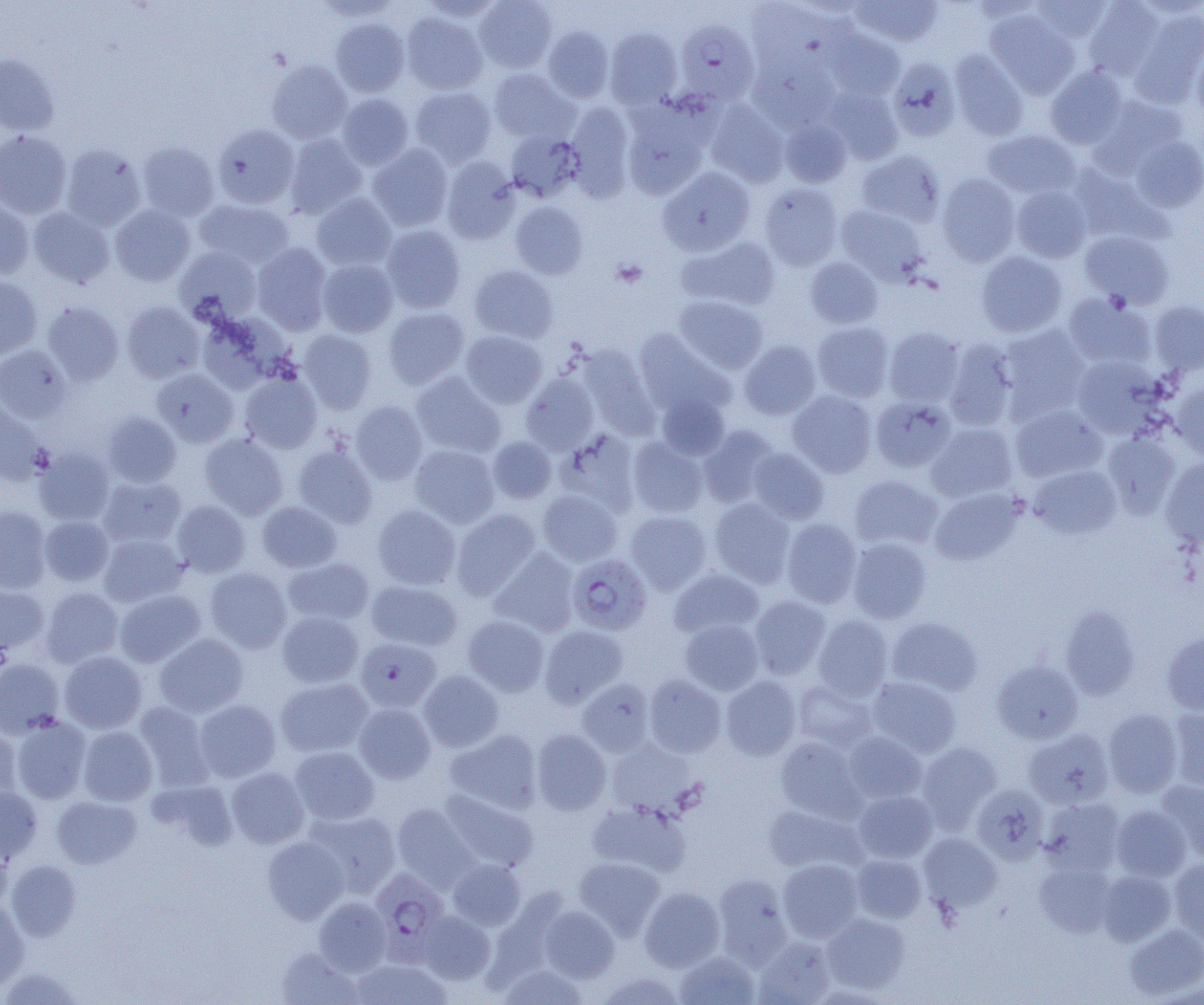 Approximate bounding boxes as [x1, y1, x2, y2] in pixels. Plasmodium falciparum-infected red blood cell locations: [674, 19, 760, 106], [566, 554, 652, 636], [355, 638, 441, 713], [369, 869, 449, 962]. Uninfected red blood cell locations: [418, 0, 502, 22], [474, 0, 557, 73], [852, 0, 943, 47], [1031, 0, 1112, 43], [1083, 1, 1164, 79], [745, 2, 834, 74], [1131, 8, 1204, 106], [985, 9, 1080, 98], [401, 12, 488, 94], [330, 18, 410, 97], [543, 26, 614, 102], [822, 26, 905, 101], [604, 27, 683, 109], [1191, 45, 1204, 121], [950, 50, 1029, 141], [749, 52, 839, 132], [0, 54, 60, 135], [887, 57, 962, 142], [266, 60, 352, 143], [1046, 66, 1128, 149], [488, 68, 577, 143], [409, 87, 496, 167], [823, 87, 904, 164], [337, 94, 413, 169], [1090, 94, 1188, 176], [705, 100, 790, 188], [565, 101, 635, 199], [622, 104, 710, 199], [780, 118, 852, 188], [213, 124, 299, 208], [982, 129, 1080, 199], [0, 130, 72, 218], [505, 130, 584, 202], [284, 134, 366, 219], [1130, 135, 1204, 212], [137, 142, 219, 220], [61, 144, 146, 231], [368, 144, 452, 231], [856, 150, 945, 226], [441, 157, 520, 244], [1068, 163, 1168, 245], [658, 166, 755, 256], [936, 174, 1020, 266], [759, 183, 844, 271], [1011, 185, 1092, 263], [312, 193, 396, 271], [0, 198, 34, 279], [194, 199, 294, 270], [511, 201, 588, 279], [110, 204, 195, 286], [836, 204, 927, 283], [28, 207, 114, 288], [381, 224, 466, 313], [1079, 230, 1173, 307], [677, 237, 781, 311], [252, 242, 332, 334], [175, 247, 261, 324], [975, 251, 1067, 337], [805, 257, 883, 328], [318, 259, 398, 337], [469, 264, 558, 343], [0, 276, 42, 360], [1062, 292, 1157, 370], [674, 295, 768, 374], [1149, 300, 1204, 375], [43, 301, 124, 385], [122, 301, 204, 383], [383, 307, 470, 389], [195, 311, 289, 393], [812, 322, 893, 402], [999, 324, 1091, 419], [884, 327, 965, 406], [299, 329, 377, 414], [633, 329, 734, 419], [460, 330, 547, 408], [942, 338, 1018, 430], [739, 340, 821, 420], [0, 345, 71, 422], [576, 345, 659, 436], [1072, 355, 1164, 438], [151, 369, 239, 446], [240, 372, 322, 454], [411, 372, 505, 458], [521, 373, 599, 453], [1170, 382, 1204, 459], [787, 389, 877, 477], [656, 392, 730, 460], [871, 396, 956, 472], [351, 400, 427, 485], [0, 402, 48, 484], [1010, 404, 1108, 483], [103, 412, 181, 487], [927, 422, 1017, 502], [698, 425, 780, 507], [557, 429, 641, 516], [1101, 432, 1180, 518], [199, 433, 288, 519], [488, 436, 557, 503], [627, 437, 708, 517], [293, 444, 377, 529], [410, 444, 499, 527], [33, 447, 115, 525], [748, 448, 829, 524], [1161, 457, 1204, 551], [1028, 464, 1121, 540], [849, 475, 942, 550], [98, 476, 186, 547], [930, 488, 1023, 565], [538, 489, 622, 566], [710, 498, 795, 587], [172, 500, 250, 577], [257, 501, 341, 573], [372, 504, 460, 590], [0, 505, 51, 593], [452, 509, 541, 600], [625, 510, 713, 594], [40, 516, 113, 585], [781, 518, 862, 608], [99, 534, 187, 606], [847, 537, 932, 623], [489, 548, 580, 636], [283, 558, 375, 626], [205, 567, 291, 652], [668, 568, 763, 639], [366, 580, 463, 651], [0, 585, 48, 654], [40, 587, 123, 667], [114, 589, 206, 667], [749, 595, 831, 679], [1059, 605, 1140, 700], [277, 611, 364, 688], [462, 615, 549, 696], [812, 615, 893, 700], [886, 617, 983, 696], [679, 618, 763, 695], [539, 625, 628, 707], [1162, 631, 1204, 716], [154, 633, 248, 717], [59, 651, 147, 733], [0, 659, 64, 737], [992, 660, 1083, 744], [418, 670, 504, 751], [644, 674, 726, 757], [721, 675, 801, 760], [867, 676, 961, 757], [274, 677, 373, 757], [576, 678, 655, 757], [792, 680, 877, 751], [194, 700, 281, 782], [134, 701, 214, 790], [353, 703, 436, 783], [1103, 708, 1183, 797], [1166, 708, 1204, 792], [10, 715, 91, 804], [78, 726, 157, 805], [0, 727, 21, 803], [1024, 728, 1114, 809], [445, 729, 543, 814], [531, 729, 611, 815], [842, 731, 927, 804], [775, 736, 864, 821], [606, 739, 698, 816], [916, 742, 1002, 831], [289, 746, 379, 825], [227, 768, 309, 848], [149, 780, 239, 850], [1155, 780, 1204, 862], [971, 783, 1050, 864], [0, 786, 42, 864], [440, 789, 538, 872], [854, 790, 937, 862], [52, 796, 141, 868], [1039, 796, 1125, 875], [587, 799, 692, 877], [392, 803, 478, 890], [763, 804, 865, 874], [1111, 805, 1191, 881], [303, 809, 400, 897], [919, 832, 1002, 911], [262, 836, 349, 924], [0, 839, 12, 912], [851, 854, 926, 922], [573, 857, 665, 940], [447, 858, 526, 930], [1169, 858, 1204, 942], [778, 859, 863, 942], [5, 860, 81, 941], [1034, 861, 1116, 936], [1096, 870, 1176, 945], [712, 874, 793, 967], [639, 887, 725, 971], [314, 897, 391, 975], [0, 899, 29, 990], [539, 906, 619, 983], [417, 910, 496, 984], [821, 913, 909, 993], [1124, 924, 1204, 999], [754, 936, 837, 1004], [275, 947, 362, 1005], [674, 950, 759, 1004], [350, 958, 451, 1005], [498, 963, 589, 1005], [1, 968, 82, 1004], [597, 971, 686, 1005]. Platelet locations: [611, 260, 648, 288]. Slide-level diagnosis: Plasmodium falciparum. Light microscopy. Thin blood film. Image is 1204×1005 pixels. 1000x magnification. One field of a larger specimen.